Locate every parasitized red blood cell.
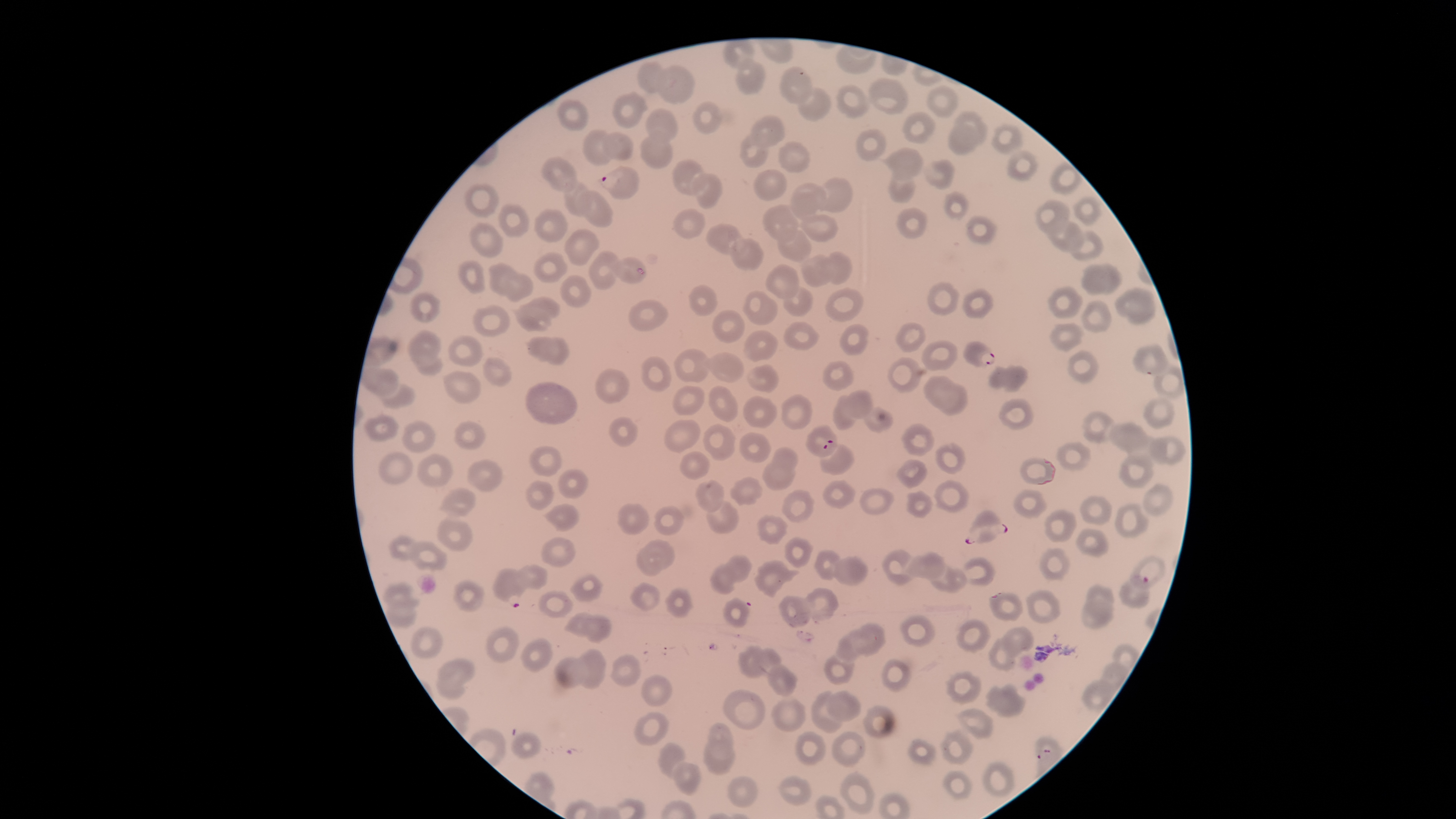
Approximate bounding boxes, in pixels from the top-left corner.
Parasitized red blood cells: (left=598, top=165, right=640, bottom=200), (left=962, top=341, right=996, bottom=368), (left=1132, top=344, right=1171, bottom=376), (left=805, top=424, right=838, bottom=458), (left=965, top=509, right=1008, bottom=544), (left=492, top=567, right=528, bottom=608), (left=1118, top=574, right=1150, bottom=608).

image size = 1456×819 pixels
capture = smartphone photograph through the microscope eyepiece
visible region = circular
stain = Giemsa
uninfected red blood cells = approximate bounding boxes, in pixels from the top-left corner: (left=736, top=57, right=765, bottom=95), (left=637, top=60, right=668, bottom=93), (left=657, top=65, right=695, bottom=105), (left=779, top=65, right=814, bottom=104), (left=867, top=77, right=909, bottom=116), (left=835, top=84, right=869, bottom=120), (left=926, top=84, right=959, bottom=119), (left=798, top=87, right=831, bottom=121), (left=612, top=91, right=650, bottom=129), (left=558, top=99, right=589, bottom=132), (left=693, top=101, right=722, bottom=135), (left=645, top=108, right=678, bottom=141), (left=954, top=110, right=988, bottom=143), (left=901, top=112, right=936, bottom=144), (left=749, top=114, right=786, bottom=148), (left=990, top=122, right=1022, bottom=155), (left=946, top=123, right=983, bottom=155), (left=582, top=128, right=614, bottom=165), (left=856, top=129, right=887, bottom=162), (left=603, top=131, right=634, bottom=162), (left=639, top=132, right=672, bottom=170), (left=739, top=134, right=768, bottom=168), (left=778, top=141, right=811, bottom=173), (left=880, top=147, right=922, bottom=177), (left=1007, top=150, right=1038, bottom=182), (left=541, top=157, right=577, bottom=193), (left=672, top=159, right=707, bottom=196), (left=924, top=160, right=955, bottom=190), (left=1049, top=162, right=1082, bottom=195), (left=753, top=168, right=787, bottom=202), (left=887, top=170, right=916, bottom=204), (left=693, top=173, right=723, bottom=210), (left=816, top=178, right=854, bottom=213), (left=563, top=181, right=590, bottom=217), (left=464, top=182, right=500, bottom=218), (left=789, top=183, right=828, bottom=220), (left=578, top=190, right=614, bottom=227), (left=943, top=191, right=970, bottom=221), (left=1073, top=196, right=1102, bottom=226), (left=1034, top=200, right=1071, bottom=234), (left=497, top=202, right=530, bottom=238), (left=763, top=204, right=799, bottom=244), (left=896, top=207, right=927, bottom=239), (left=672, top=208, right=705, bottom=239), (left=533, top=209, right=568, bottom=243), (left=799, top=214, right=838, bottom=242), (left=965, top=216, right=997, bottom=244), (left=1048, top=219, right=1086, bottom=252), (left=468, top=222, right=504, bottom=257), (left=706, top=224, right=745, bottom=254), (left=564, top=228, right=600, bottom=266), (left=777, top=229, right=813, bottom=263), (left=1070, top=231, right=1106, bottom=260), (left=730, top=238, right=764, bottom=270), (left=827, top=250, right=852, bottom=284), (left=532, top=251, right=569, bottom=283), (left=589, top=251, right=620, bottom=290), (left=800, top=254, right=834, bottom=288), (left=612, top=256, right=646, bottom=284), (left=457, top=260, right=486, bottom=295), (left=488, top=262, right=519, bottom=295), (left=1080, top=263, right=1124, bottom=296), (left=765, top=264, right=800, bottom=300), (left=505, top=273, right=533, bottom=302), (left=560, top=275, right=591, bottom=308), (left=927, top=281, right=960, bottom=316), (left=689, top=283, right=718, bottom=316), (left=1047, top=285, right=1083, bottom=319), (left=783, top=286, right=812, bottom=318), (left=1114, top=286, right=1157, bottom=326), (left=825, top=288, right=864, bottom=323), (left=962, top=288, right=994, bottom=319), (left=409, top=291, right=441, bottom=324), (left=742, top=291, right=777, bottom=326), (left=523, top=296, right=561, bottom=320), (left=629, top=298, right=668, bottom=331), (left=1080, top=299, right=1112, bottom=334), (left=514, top=304, right=551, bottom=332), (left=472, top=305, right=512, bottom=338), (left=711, top=310, right=746, bottom=344), (left=782, top=322, right=818, bottom=350), (left=895, top=322, right=926, bottom=353), (left=1049, top=323, right=1085, bottom=352), (left=839, top=324, right=869, bottom=356), (left=407, top=330, right=441, bottom=367), (left=744, top=330, right=778, bottom=362), (left=448, top=333, right=483, bottom=367), (left=526, top=336, right=570, bottom=364), (left=921, top=341, right=958, bottom=372), (left=674, top=349, right=709, bottom=382), (left=1067, top=350, right=1099, bottom=385), (left=704, top=352, right=745, bottom=383), (left=415, top=353, right=443, bottom=376), (left=640, top=356, right=672, bottom=393), (left=482, top=357, right=512, bottom=387), (left=888, top=357, right=923, bottom=393), (left=822, top=361, right=854, bottom=392), (left=746, top=364, right=779, bottom=393), (left=988, top=364, right=1029, bottom=392), (left=1153, top=365, right=1186, bottom=399), (left=365, top=368, right=399, bottom=396), (left=596, top=369, right=630, bottom=404), (left=443, top=370, right=482, bottom=404), (left=923, top=374, right=953, bottom=408), (left=379, top=382, right=415, bottom=409), (left=525, top=382, right=578, bottom=425), (left=939, top=383, right=967, bottom=416), (left=707, top=384, right=739, bottom=422), (left=672, top=385, right=705, bottom=414), (left=844, top=390, right=874, bottom=420), (left=781, top=393, right=813, bottom=431), (left=832, top=394, right=857, bottom=431), (left=742, top=395, right=778, bottom=429), (left=1142, top=396, right=1176, bottom=430), (left=998, top=398, right=1034, bottom=431), (left=865, top=407, right=894, bottom=435), (left=1081, top=411, right=1115, bottom=443), (left=363, top=413, right=400, bottom=442), (left=609, top=416, right=640, bottom=446), (left=402, top=419, right=437, bottom=453), (left=663, top=419, right=701, bottom=453), (left=454, top=421, right=486, bottom=450), (left=1108, top=422, right=1149, bottom=453), (left=703, top=423, right=737, bottom=461), (left=901, top=423, right=936, bottom=457), (left=739, top=431, right=772, bottom=463), (left=1150, top=435, right=1187, bottom=466), (left=1056, top=441, right=1091, bottom=472), (left=936, top=442, right=966, bottom=474), (left=819, top=444, right=855, bottom=475), (left=529, top=446, right=562, bottom=477), (left=772, top=447, right=798, bottom=472), (left=378, top=450, right=413, bottom=484), (left=680, top=450, right=711, bottom=480), (left=415, top=453, right=454, bottom=489), (left=1119, top=455, right=1154, bottom=490), (left=1020, top=457, right=1056, bottom=486), (left=467, top=458, right=503, bottom=492), (left=895, top=459, right=928, bottom=488), (left=763, top=461, right=795, bottom=490), (left=557, top=469, right=588, bottom=499), (left=730, top=476, right=763, bottom=506), (left=822, top=479, right=856, bottom=509), (left=933, top=479, right=970, bottom=513), (left=525, top=480, right=555, bottom=510), (left=695, top=480, right=725, bottom=513), (left=1142, top=483, right=1174, bottom=518), (left=438, top=488, right=477, bottom=516), (left=859, top=488, right=895, bottom=515), (left=782, top=489, right=814, bottom=523), (left=1013, top=489, right=1047, bottom=519), (left=906, top=490, right=933, bottom=518), (left=1079, top=495, right=1112, bottom=525), (left=706, top=500, right=739, bottom=535), (left=617, top=503, right=650, bottom=535), (left=1115, top=503, right=1149, bottom=538), (left=545, top=504, right=579, bottom=531), (left=654, top=505, right=683, bottom=536), (left=1043, top=509, right=1076, bottom=542), (left=756, top=514, right=788, bottom=545), (left=437, top=518, right=474, bottom=553), (left=1075, top=527, right=1108, bottom=557), (left=388, top=535, right=417, bottom=561), (left=540, top=535, right=577, bottom=567), (left=784, top=535, right=813, bottom=568), (left=645, top=539, right=676, bottom=570), (left=408, top=540, right=447, bottom=572), (left=636, top=546, right=664, bottom=577), (left=1039, top=547, right=1070, bottom=581), (left=813, top=549, right=841, bottom=581), (left=881, top=549, right=915, bottom=585), (left=903, top=551, right=946, bottom=580), (left=723, top=553, right=753, bottom=582), (left=834, top=554, right=868, bottom=586), (left=1131, top=555, right=1167, bottom=589), (left=961, top=557, right=997, bottom=586), (left=754, top=559, right=801, bottom=598), (left=520, top=563, right=548, bottom=590), (left=708, top=563, right=737, bottom=595), (left=930, top=564, right=966, bottom=593), (left=570, top=573, right=604, bottom=603), (left=453, top=580, right=484, bottom=612), (left=381, top=581, right=420, bottom=608), (left=629, top=582, right=661, bottom=611), (left=1086, top=584, right=1114, bottom=611), (left=804, top=586, right=838, bottom=621), (left=664, top=588, right=694, bottom=617), (left=1025, top=589, right=1061, bottom=624), (left=537, top=590, right=574, bottom=619), (left=988, top=591, right=1023, bottom=621), (left=779, top=595, right=811, bottom=628), (left=723, top=596, right=751, bottom=628), (left=385, top=599, right=417, bottom=627), (left=1080, top=601, right=1114, bottom=630), (left=564, top=612, right=596, bottom=637), (left=899, top=613, right=936, bottom=648), (left=584, top=615, right=613, bottom=644), (left=955, top=618, right=991, bottom=654), (left=855, top=622, right=887, bottom=656), (left=485, top=625, right=520, bottom=663), (left=1000, top=625, right=1034, bottom=656), (left=411, top=626, right=444, bottom=659), (left=836, top=630, right=867, bottom=661), (left=988, top=636, right=1017, bottom=671), (left=520, top=638, right=553, bottom=672), (left=737, top=644, right=766, bottom=679), (left=1113, top=644, right=1139, bottom=671), (left=578, top=647, right=606, bottom=690), (left=756, top=647, right=783, bottom=673), (left=609, top=653, right=640, bottom=687), (left=823, top=653, right=855, bottom=685), (left=554, top=656, right=585, bottom=689), (left=882, top=657, right=912, bottom=692), (left=437, top=658, right=475, bottom=691), (left=1101, top=662, right=1129, bottom=691), (left=766, top=664, right=798, bottom=698), (left=945, top=671, right=982, bottom=705), (left=640, top=673, right=672, bottom=707), (left=1081, top=679, right=1115, bottom=712), (left=984, top=682, right=1026, bottom=718), (left=721, top=689, right=765, bottom=730), (left=810, top=690, right=843, bottom=733), (left=825, top=690, right=862, bottom=721), (left=771, top=696, right=807, bottom=731), (left=862, top=705, right=897, bottom=740), (left=954, top=708, right=994, bottom=741), (left=634, top=711, right=669, bottom=745), (left=708, top=722, right=735, bottom=760), (left=937, top=727, right=973, bottom=765), (left=794, top=730, right=828, bottom=765), (left=510, top=731, right=541, bottom=759), (left=831, top=731, right=866, bottom=767), (left=907, top=737, right=936, bottom=765), (left=703, top=738, right=735, bottom=775), (left=658, top=742, right=686, bottom=779), (left=981, top=761, right=1016, bottom=797), (left=671, top=762, right=702, bottom=798), (left=942, top=769, right=972, bottom=800), (left=839, top=771, right=876, bottom=816), (left=727, top=775, right=759, bottom=809), (left=778, top=775, right=812, bottom=806)
preparation = thin blood film
field of view = single
species = Plasmodium falciparum